Give the extent of all Plasmodium falciparum-infected red blood cells.
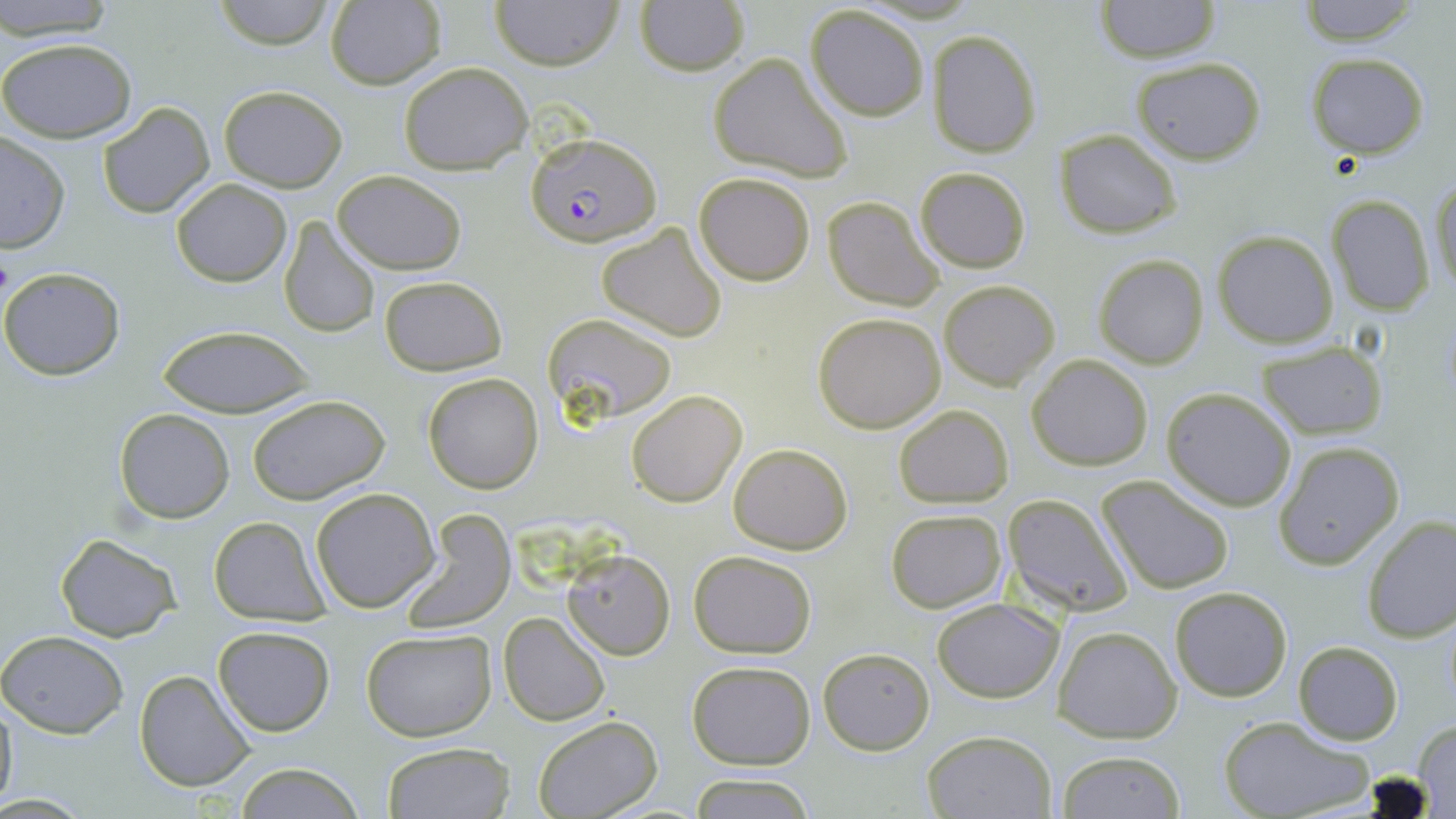

Approximate bounding boxes as (x1,y1)-(x2,y2) corner pairs in pixels.
Plasmodium falciparum-infected red blood cells: (526,132)-(664,247).

slide-level diagnosis = Plasmodium falciparum
uninfected red blood cell locations = approximate bounding boxes as (x1,y1)-(x2,y2) corner pairs in pixels: (0,0)-(119,41), (208,0)-(338,49), (490,0)-(624,72), (1096,0)-(1221,64), (1296,0)-(1424,45), (323,1)-(447,89), (635,1)-(749,75), (805,5)-(930,120), (927,28)-(1040,157), (0,36)-(137,144), (707,53)-(852,183), (1305,53)-(1430,158), (1131,57)-(1265,166), (397,62)-(533,175), (218,85)-(348,191), (98,102)-(214,220), (1055,129)-(1181,239), (0,135)-(70,254), (914,166)-(1031,273), (332,170)-(468,274), (693,172)-(817,285), (1429,173)-(1456,299), (171,178)-(291,286), (1325,193)-(1437,317), (821,195)-(945,311), (277,217)-(383,340), (596,222)-(729,340), (1214,230)-(1338,347), (1094,254)-(1209,368), (0,266)-(126,380), (379,275)-(507,375), (938,280)-(1059,390), (541,312)-(678,429), (812,312)-(947,433), (155,326)-(317,417), (1256,341)-(1387,438), (1027,354)-(1153,471), (422,372)-(543,493), (1161,387)-(1297,511), (626,390)-(747,508), (244,394)-(391,505), (893,403)-(1014,508), (114,408)-(236,523), (1272,441)-(1404,570), (729,442)-(852,553), (1097,475)-(1233,596), (310,487)-(440,611), (1001,493)-(1135,616), (885,506)-(1009,614), (397,509)-(516,632), (1360,514)-(1456,642), (209,515)-(330,623), (54,534)-(183,641), (561,549)-(675,659), (688,550)-(818,658), (1170,585)-(1293,700), (932,598)-(1061,701), (499,612)-(610,727), (213,625)-(335,738), (1053,625)-(1184,744), (360,629)-(497,742), (0,630)-(129,738), (1294,641)-(1402,745), (819,648)-(934,753), (686,660)-(817,769), (134,669)-(255,792), (1,691)-(19,816), (532,715)-(662,819), (1218,715)-(1373,819), (1412,717)-(1456,814), (922,729)-(1057,818), (380,742)-(515,819), (1057,751)-(1185,818), (231,763)-(370,818), (689,773)-(815,818)
image size = 1456×819 pixels
magnification = 1000x
modality = optical microscopy
field of view = one of a larger specimen
preparation = thin blood film
stain = May-Grünwald-Giemsa